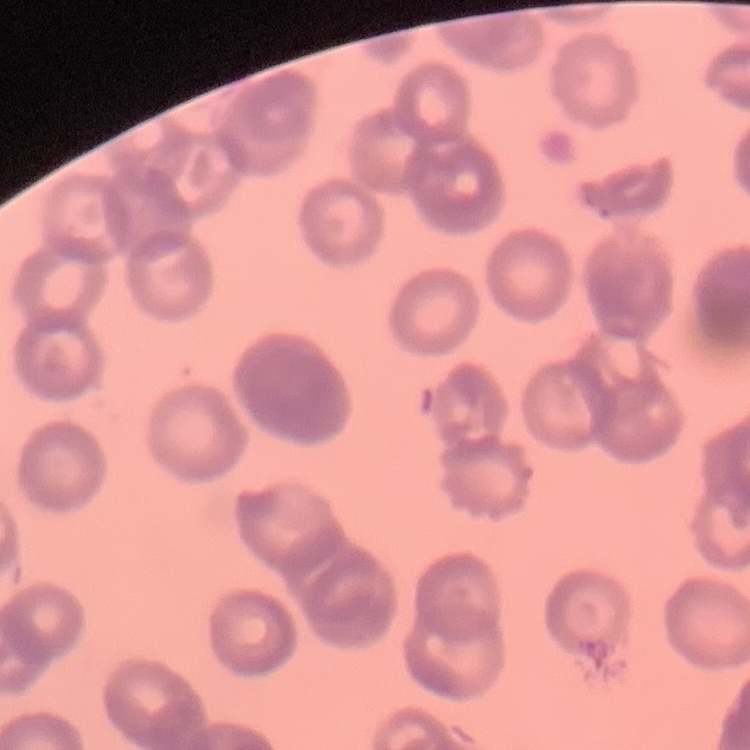
erythrocyte morphology = rouleaux formation
preparation = thin blood film
stain = Field's or Giemsa
image type = square crop of a larger photomicrograph